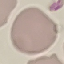

Summary:
  - Result: negative for malaria parasites
  - Image type: cell patch, automatically extracted from a larger field of view and resized to 64 × 64 pixels
  - Capture: smartphone through the microscope eyepiece
  - Stain: Giemsa
  - Preparation: thin blood smear